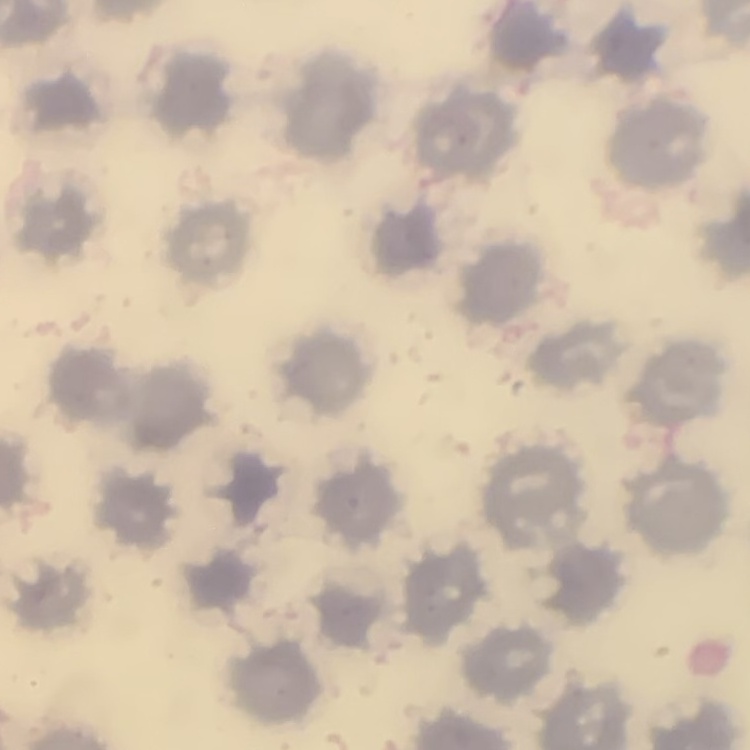
Summary:
  - Red blood cell morphology: no rouleaux formation
  - Stain: Field's or Giemsa
  - Image type: square crop of a larger photomicrograph
  - Preparation: thin peripheral smear